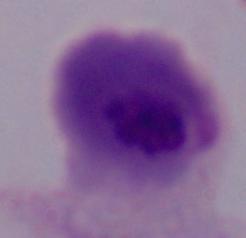
Summary:
  - Magnification: 1000x
  - Modality: micrograph
  - Identification: trichomonad